Point out every Plasmodium parasite.
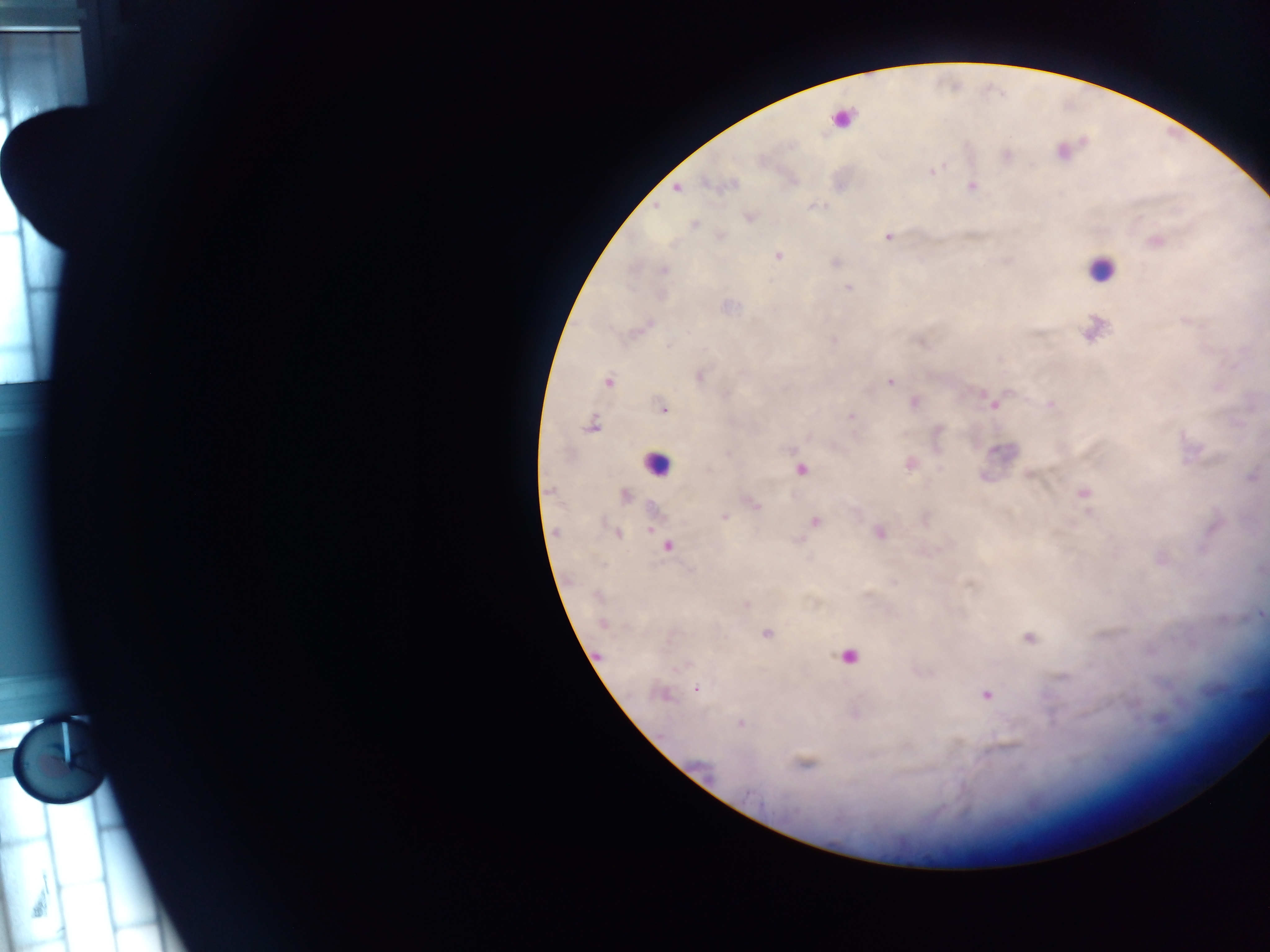

Approximate centers as {x, y} in pixels.
Plasmodium parasites: {733, 184}, {677, 188}, {656, 206}, {750, 217}, {695, 224}, {888, 237}, {778, 256}, {664, 270}, {848, 287}, {699, 377}, {608, 382}, {889, 382}, {993, 404}, {1051, 404}, {664, 409}, {851, 416}, {590, 426}, {800, 469}, {1251, 476}, {548, 490}, {1083, 493}, {625, 495}, {756, 506}, {724, 517}, {815, 522}, {651, 529}, {617, 533}, {879, 533}, {667, 546}, {747, 604}, {1261, 614}, {603, 624}, {766, 634}, {1029, 638}, {696, 689}, {986, 695}, {662, 696}, {740, 723}, {806, 763}, {751, 795}.

Summary:
  - Leukocyte locations (subset; some below the resolvable size): {842, 119}, {1100, 269}, {656, 464}, {848, 657}
  - Image size: 1270×952 pixels
  - Capture: mobile-phone photograph through a microscope
  - Field of view: single
  - Country: Ghana
  - Preparation: thick blood film